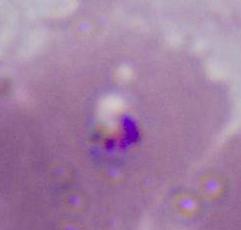

identification = Plasmodium
magnification = 400x or 1000x
modality = micrograph